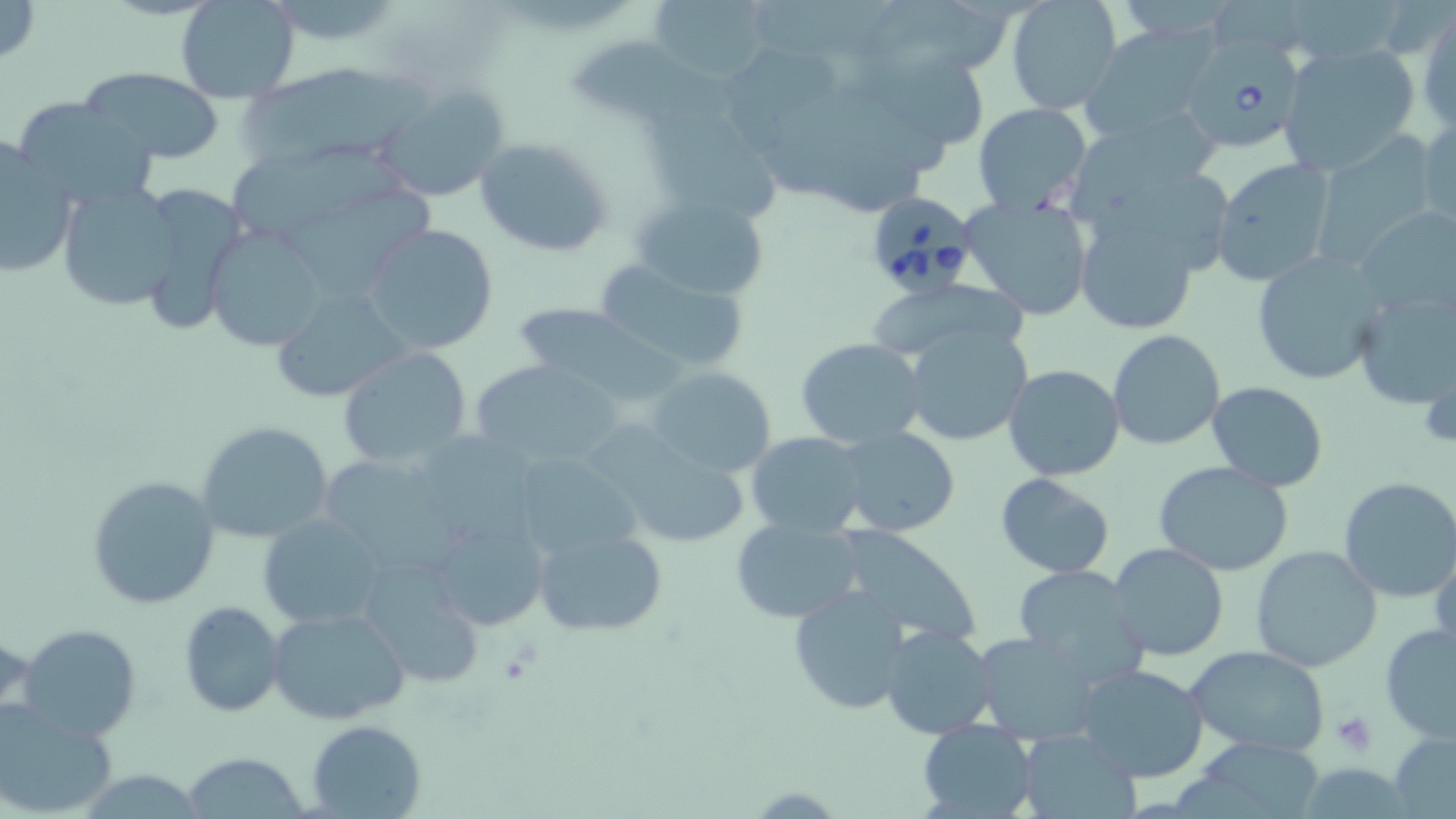

Summary:
  - Coordinate format: approximate bounding boxes as named x1/y1/x2/y2 corners in pixels
  - Uninfected red blood cell locations: (x1=0, y1=0, x2=41, y2=68), (x1=176, y1=0, x2=302, y2=102), (x1=647, y1=0, x2=774, y2=85), (x1=868, y1=0, x2=1007, y2=71), (x1=1005, y1=0, x2=1122, y2=114), (x1=1417, y1=11, x2=1455, y2=128), (x1=1080, y1=28, x2=1222, y2=143), (x1=866, y1=37, x2=994, y2=145), (x1=577, y1=41, x2=751, y2=132), (x1=1278, y1=42, x2=1421, y2=175), (x1=725, y1=43, x2=849, y2=134), (x1=240, y1=62, x2=443, y2=160), (x1=77, y1=68, x2=225, y2=164), (x1=370, y1=83, x2=510, y2=201), (x1=10, y1=97, x2=157, y2=210), (x1=973, y1=102, x2=1092, y2=216), (x1=648, y1=107, x2=786, y2=218), (x1=1073, y1=111, x2=1219, y2=221), (x1=1416, y1=113, x2=1455, y2=235), (x1=1311, y1=133, x2=1439, y2=262), (x1=0, y1=136, x2=79, y2=279), (x1=474, y1=137, x2=615, y2=257), (x1=236, y1=153, x2=409, y2=231), (x1=1210, y1=157, x2=1337, y2=287), (x1=1082, y1=175, x2=1243, y2=278), (x1=56, y1=180, x2=184, y2=311), (x1=133, y1=180, x2=248, y2=336), (x1=1070, y1=183, x2=1218, y2=338), (x1=287, y1=187, x2=435, y2=293), (x1=631, y1=191, x2=773, y2=303), (x1=959, y1=195, x2=1095, y2=319), (x1=1355, y1=205, x2=1456, y2=316), (x1=361, y1=224, x2=499, y2=356), (x1=205, y1=226, x2=329, y2=351), (x1=1249, y1=250, x2=1386, y2=384), (x1=591, y1=259, x2=751, y2=376), (x1=868, y1=282, x2=1041, y2=355), (x1=268, y1=286, x2=413, y2=405), (x1=1350, y1=286, x2=1455, y2=410), (x1=509, y1=304, x2=671, y2=401), (x1=900, y1=321, x2=1033, y2=447), (x1=1106, y1=329, x2=1226, y2=450), (x1=794, y1=338, x2=927, y2=450), (x1=335, y1=344, x2=474, y2=471), (x1=470, y1=358, x2=626, y2=471), (x1=1003, y1=364, x2=1126, y2=481), (x1=645, y1=365, x2=778, y2=480), (x1=1207, y1=380, x2=1327, y2=492), (x1=195, y1=420, x2=335, y2=544), (x1=583, y1=422, x2=760, y2=555), (x1=835, y1=429, x2=958, y2=537), (x1=746, y1=431, x2=870, y2=536), (x1=433, y1=436, x2=535, y2=554), (x1=508, y1=454, x2=641, y2=564), (x1=328, y1=460, x2=467, y2=578), (x1=1153, y1=460, x2=1295, y2=576), (x1=994, y1=473, x2=1115, y2=579), (x1=86, y1=474, x2=222, y2=609), (x1=1338, y1=476, x2=1456, y2=601), (x1=258, y1=513, x2=388, y2=630), (x1=427, y1=516, x2=551, y2=633), (x1=729, y1=516, x2=863, y2=625), (x1=833, y1=526, x2=983, y2=645), (x1=534, y1=528, x2=667, y2=636), (x1=1431, y1=540, x2=1456, y2=660), (x1=1107, y1=542, x2=1230, y2=662), (x1=1250, y1=545, x2=1383, y2=670), (x1=357, y1=557, x2=488, y2=690), (x1=1011, y1=565, x2=1147, y2=682), (x1=787, y1=583, x2=918, y2=714), (x1=177, y1=600, x2=286, y2=717), (x1=264, y1=605, x2=414, y2=727), (x1=1380, y1=622, x2=1456, y2=743), (x1=17, y1=623, x2=143, y2=743), (x1=881, y1=625, x2=998, y2=738), (x1=972, y1=631, x2=1105, y2=742), (x1=1186, y1=645, x2=1331, y2=758), (x1=1076, y1=663, x2=1210, y2=783), (x1=0, y1=702, x2=120, y2=817), (x1=306, y1=719, x2=427, y2=819), (x1=915, y1=719, x2=1038, y2=819), (x1=1018, y1=728, x2=1137, y2=818), (x1=1389, y1=732, x2=1456, y2=819), (x1=1205, y1=739, x2=1319, y2=819), (x1=183, y1=751, x2=309, y2=818)
  - Babesia divergens-infected red blood cell locations: (x1=1191, y1=36, x2=1303, y2=150), (x1=864, y1=191, x2=977, y2=297)
  - Platelet locations: (x1=1332, y1=712, x2=1376, y2=756)
  - Slide-level diagnosis: Babesia divergens
  - Preparation: thin blood film
  - Stain: May-Grünwald-Giemsa
  - Field of view: single
  - Modality: light microscopy
  - Image size: 1456×819 pixels
  - Magnification: 1000x